Assess this cell for malaria.
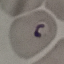
Parasitized.

Summary:
  - Stain: Giemsa
  - Preparation: thin blood smear
  - Image type: automatically extracted cell patch, resized to 64 × 64 pixels
  - Capture: smartphone through the microscope eyepiece